Report the malaria status of this cell.
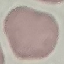

It is uninfected.

{
  "image_type": "automatically extracted cell patch, resized to 64 × 64 pixels",
  "preparation": "thin smear",
  "stain": "Giemsa",
  "capture": "smartphone through the microscope eyepiece"
}